Locate every Plasmodium parasite.
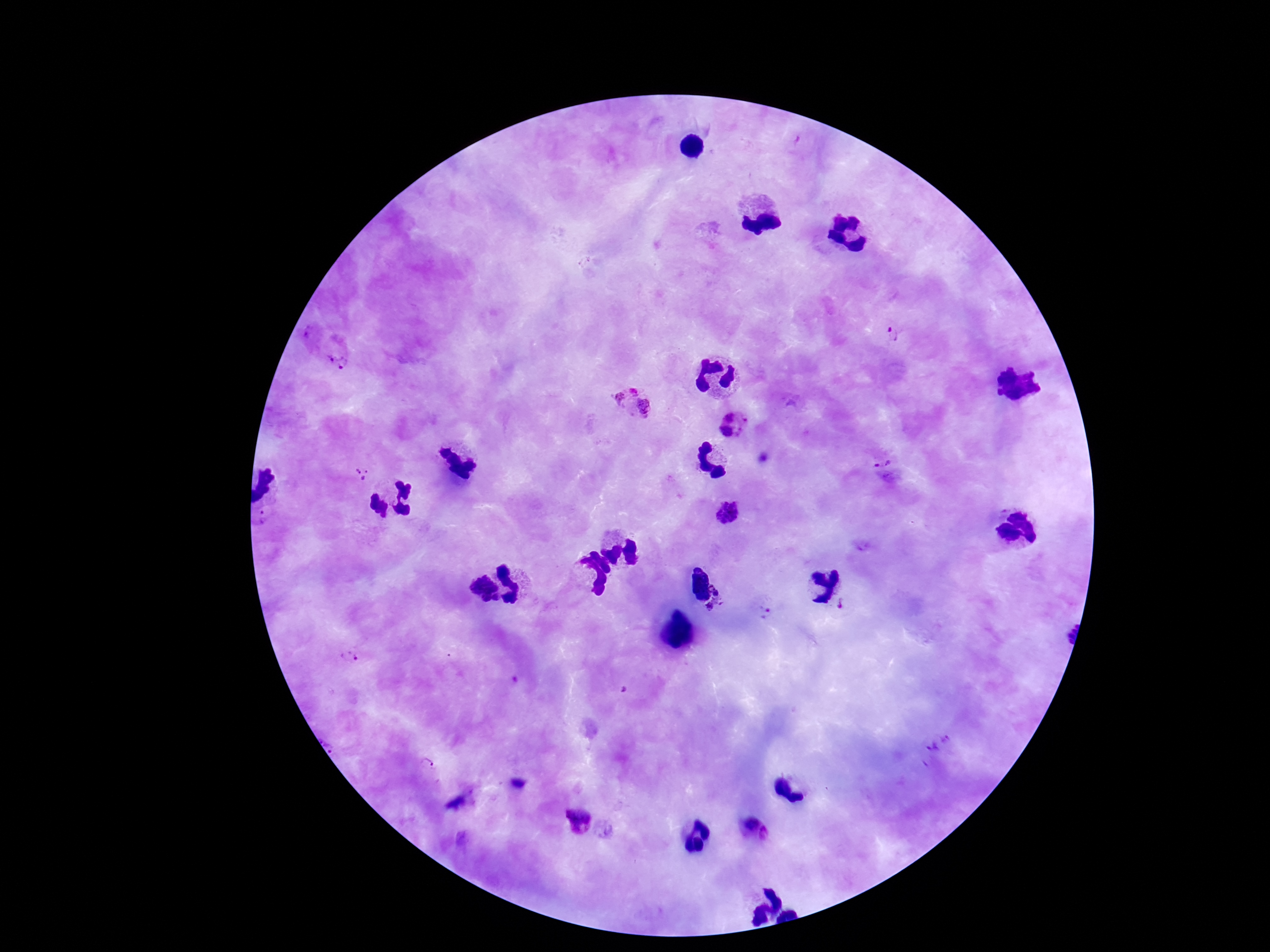

Approximate centers as (x, y) in pixels.
Plasmodium parasites: (893, 333), (338, 353), (632, 401), (733, 426), (883, 461), (361, 471), (725, 515), (266, 517), (724, 602), (843, 605), (762, 612), (350, 658), (425, 769), (579, 821).

Image is 1270×952 pixels. Photographed through the microscope eyepiece with a smartphone camera. Single field of view. 100x magnification. Patient malaria status: positive. Giemsa stain. Thick blood film.